Classify this cell by malaria status.
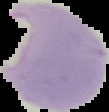

Parasitized.

image size = 109×112 pixels
image type = segmented cell region on a black background
preparation = thin blood smear